Assess for malaria.
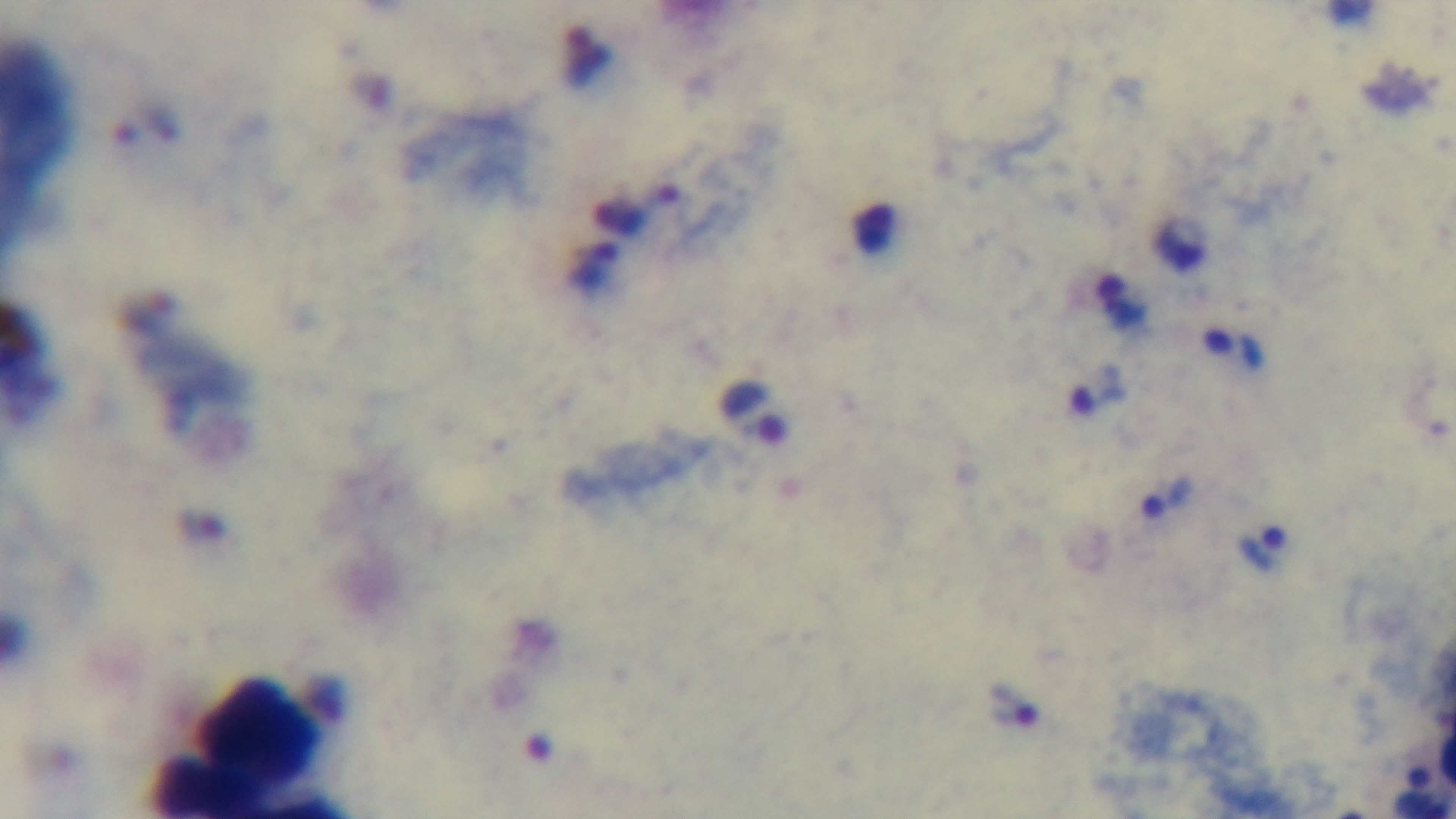
It is infected.

Giemsa stain. Photomicrograph. Oil-immersion objective, 100x. Single field of view. Captured with a mounted 4K digital camera. Preparation: thick smear.